Name the parasite shown.
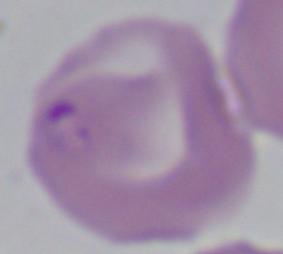
Babesia.

Summary:
  - Modality: photomicrograph
  - Magnification: 1000x